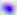
identification = Toxoplasma gondii
magnification = 400x
modality = photomicrograph